Locate every blood parasite and identify its species.
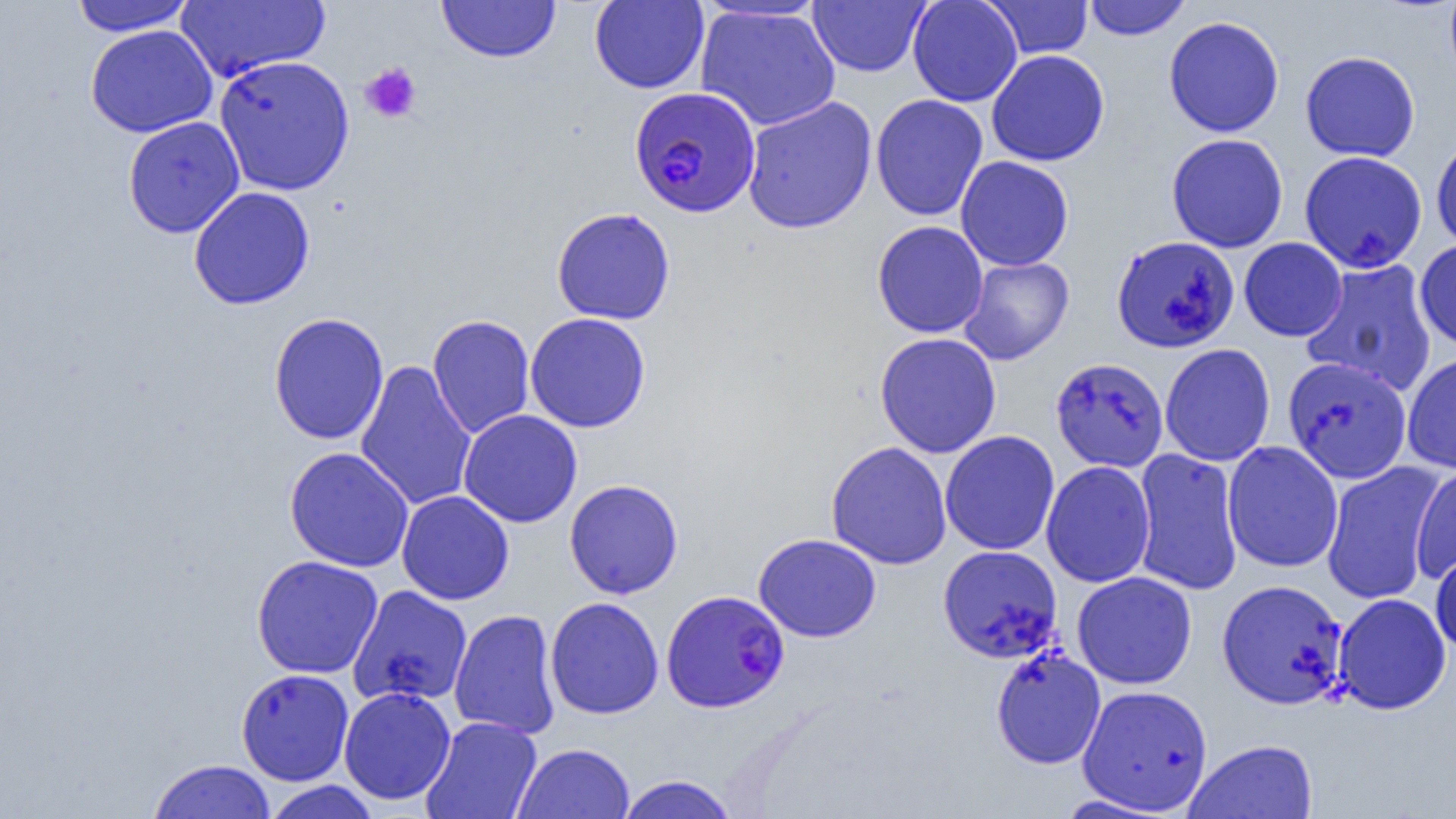

Approximate bounding boxes as (x1,y1)-(x2,y2) corner pairs in pixels.
Plasmodium falciparum-infected red blood cells: (629,86)-(761,217), (661,589)-(790,712).
No Plasmodium ovale, Plasmodium malariae, Plasmodium vivax, Babesia divergens, or Trypanosoma brucei observed.

{
  "slide_level_diagnosis": "Plasmodium falciparum",
  "platelet_locations": "approximate bounding boxes as (x1,y1)-(x2,y2) corner pairs in pixels: (359,62)-(422,124)",
  "image_size": "1456×819 pixels",
  "uninfected_red_blood_cell_locations": "approximate bounding boxes as (x1,y1)-(x2,y2) corner pairs in pixels: (69,0)-(196,36), (437,0)-(561,63), (907,0)-(1023,107), (1082,0)-(1192,40), (174,1)-(330,83), (589,1)-(709,93), (808,1)-(930,77), (983,1)-(1093,59), (695,5)-(840,131), (1163,16)-(1285,137), (85,24)-(217,137), (986,49)-(1110,167), (1300,51)-(1420,161), (214,55)-(355,196), (870,93)-(989,221), (741,96)-(878,234), (122,116)-(245,238), (1166,133)-(1288,253), (1432,134)-(1456,253), (1299,151)-(1426,272), (955,156)-(1074,271), (188,186)-(315,309), (551,207)-(676,325), (872,220)-(989,338), (1111,235)-(1239,353), (1239,237)-(1347,342), (1415,238)-(1456,351), (958,256)-(1075,365), (1300,259)-(1438,397), (268,312)-(389,445), (524,313)-(651,433), (427,314)-(535,438), (874,332)-(1002,458), (1160,343)-(1275,466), (1402,353)-(1456,474), (1282,356)-(1412,484), (1051,357)-(1169,471), (355,359)-(477,511), (458,409)-(583,528), (940,430)-(1060,555), (826,441)-(952,570), (1222,441)-(1343,573), (284,447)-(414,572), (1132,448)-(1244,596), (1041,461)-(1156,588), (1321,461)-(1445,606), (1411,462)-(1456,583), (564,479)-(683,599), (396,490)-(514,605), (753,533)-(882,643), (937,545)-(1063,663), (1430,547)-(1456,655), (251,555)-(383,679), (1071,572)-(1197,689), (1217,578)-(1349,710), (347,585)-(473,707), (1332,593)-(1451,715), (545,596)-(664,720), (449,608)-(561,739), (990,646)-(1106,770), (236,668)-(354,786), (1076,684)-(1214,815), (339,686)-(456,805), (420,716)-(542,819), (1184,738)-(1319,819), (512,743)-(634,819), (146,759)-(276,819), (616,775)-(739,819), (262,780)-(383,818), (1053,794)-(1176,817)",
  "magnification": "1000x",
  "preparation": "thin blood smear",
  "field_of_view": "single",
  "modality": "light microscopy"
}